Assess this cell for malaria.
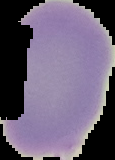
Uninfected.

Image is 115×160 pixels. Cell region segmented out of the field of view; the surrounding area is masked to black. From a thin blood smear.